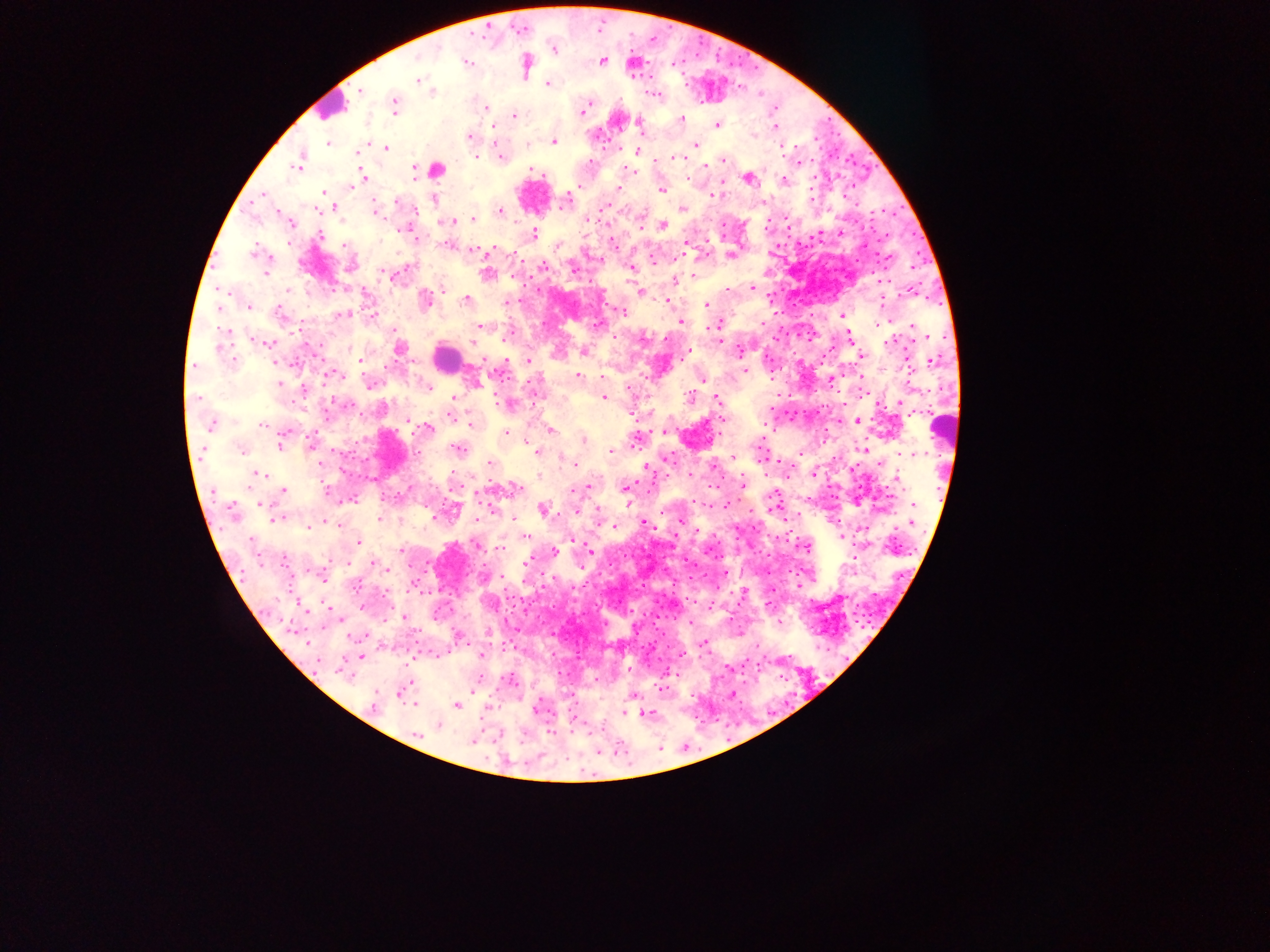
Approximate centers as (x, y) in pixels.
Summary:
  - Leukocyte locations: (330, 106), (533, 196), (445, 358), (943, 424)
  - Plasmodium parasite locations: (553, 49), (417, 59), (466, 61), (601, 61), (524, 65), (418, 80), (547, 84), (361, 90), (431, 92), (654, 94), (395, 104), (486, 107), (582, 111), (514, 115), (681, 119), (717, 123), (638, 124), (493, 125), (775, 127), (469, 137), (553, 141), (328, 143), (695, 144), (385, 148), (636, 150), (357, 153), (500, 156), (673, 157), (723, 160), (299, 162), (590, 162), (528, 168), (436, 169), (415, 171), (634, 172), (362, 177), (747, 177), (783, 180), (619, 188), (661, 189), (323, 192), (264, 195), (433, 198), (566, 199), (395, 201), (336, 207), (682, 208), (375, 211), (500, 211), (473, 219), (451, 221), (289, 223), (664, 224), (407, 227), (533, 234), (320, 235), (448, 245), (684, 245), (474, 251), (255, 252), (730, 255), (652, 261), (350, 267), (573, 269), (631, 269), (265, 271), (487, 273), (393, 275), (694, 275), (673, 281), (750, 288), (727, 290), (640, 292), (364, 294), (465, 300), (667, 300), (425, 301), (506, 303), (705, 304), (249, 305), (217, 307), (622, 312), (278, 313), (372, 313), (341, 315), (843, 315), (680, 321), (878, 324), (598, 325), (480, 326), (715, 326), (393, 328), (225, 331), (508, 334), (717, 334), (848, 334), (257, 339), (889, 341), (266, 342), (473, 344), (399, 349), (583, 351), (741, 351), (687, 354), (861, 355), (359, 359), (930, 360), (233, 361), (527, 361), (195, 366), (744, 369), (332, 374), (576, 376), (601, 377), (702, 379), (861, 379), (830, 380), (370, 383), (280, 384), (425, 385), (303, 389), (605, 397), (690, 397), (453, 398), (717, 399), (507, 403), (327, 413), (450, 415), (856, 421), (471, 424), (210, 425), (263, 425), (427, 428), (550, 429), (505, 432), (664, 432), (583, 439), (280, 442), (635, 442), (310, 443), (457, 448), (862, 448), (241, 449), (530, 449), (610, 450), (537, 452), (799, 453), (906, 453), (733, 456), (489, 463), (575, 464), (713, 465), (256, 473), (689, 474), (896, 479), (741, 484), (513, 487), (586, 487), (625, 487), (284, 489), (574, 489), (327, 491), (353, 498), (260, 504), (725, 504), (773, 505), (543, 509), (576, 511), (233, 513), (277, 518), (379, 518), (513, 518), (477, 520), (681, 520), (324, 521), (912, 521), (643, 522), (307, 526), (614, 526), (841, 535), (525, 537), (358, 541), (477, 545), (500, 548), (400, 550), (553, 550), (588, 551), (284, 560), (527, 561), (375, 564), (323, 576), (362, 606), (403, 617), (690, 623), (458, 636), (703, 642), (680, 653), (361, 655), (480, 655), (343, 668), (630, 669), (472, 685), (660, 687), (402, 692), (733, 694), (632, 696), (414, 704), (457, 704), (373, 705), (535, 708), (624, 712), (645, 714), (573, 717), (438, 725), (416, 735), (471, 741)
  - Field of view: single
  - Country: Ghana
  - Capture: mobile-phone photograph through a microscope
  - Preparation: thick blood smear
  - Image size: 1270×952 pixels